Name the parasite shown.
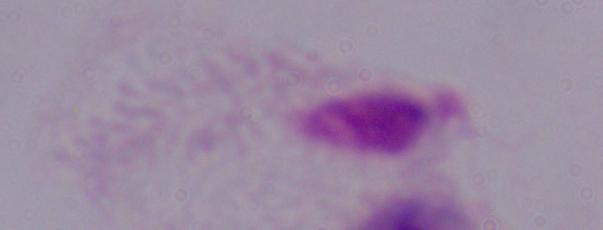

A trichomonad.

modality = photomicrograph
magnification = 1000x